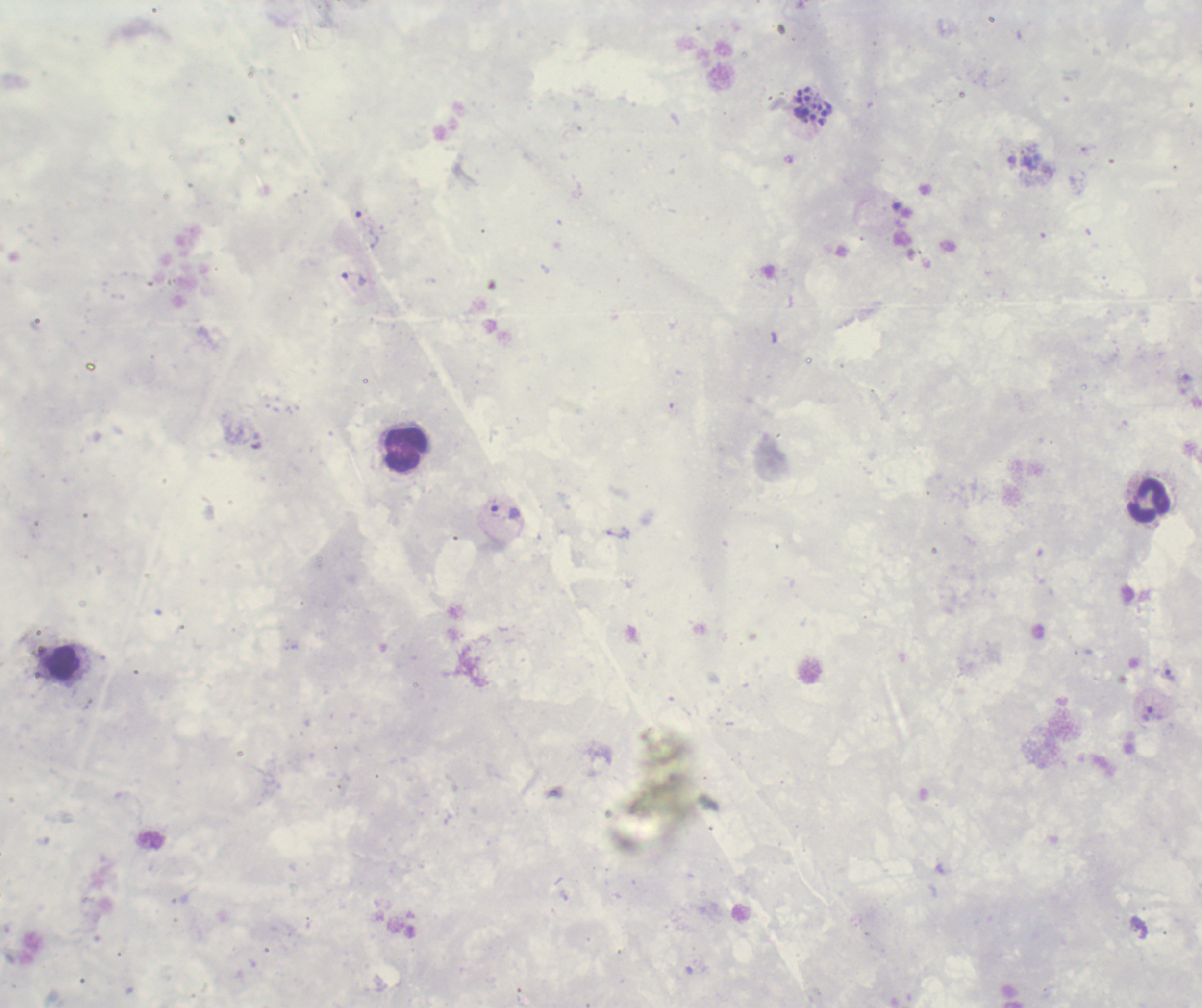

Approximate centers as (x, y) in pixels.
Summary:
  - Leukocyte locations: (406, 450), (1148, 501)
  - Schizont locations: (813, 106)
  - Trophozoite locations: (367, 229), (353, 279), (505, 512), (1168, 675), (1149, 715)
  - Life-cycle stages observed: trophozoite, schizont
  - Image size: 1202×1008 pixels
  - Stain: Romanowsky
  - Background quality: unsatisfactory
  - Result: malaria parasites identified
  - Context: previously used in an actual diagnosis
  - Magnification: 100x
  - Preparation: thick smear of blood
  - Field of view: single